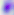
{
  "identification": "Toxoplasma gondii",
  "modality": "photomicrograph",
  "magnification": "400x"
}